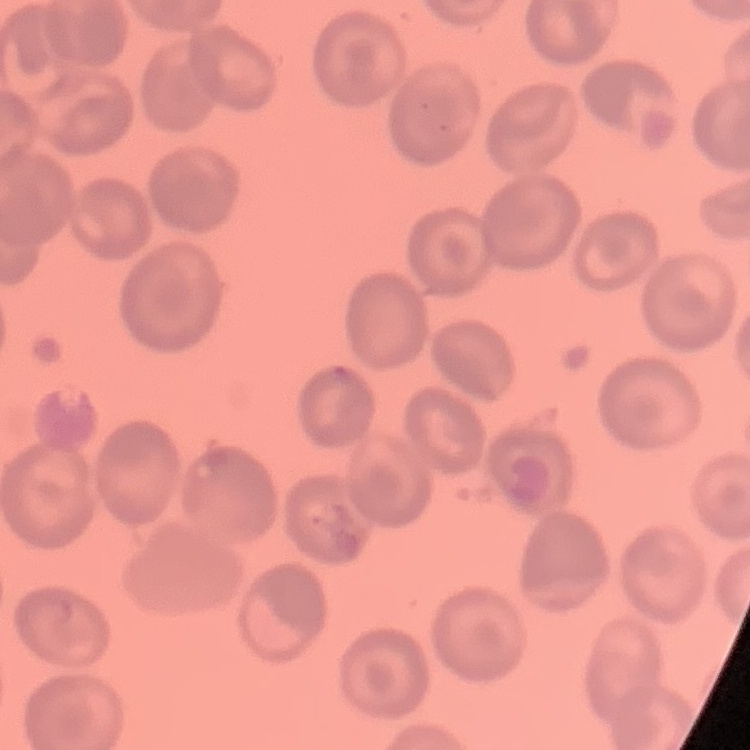 The erythrocytes exhibit no rouleaux formation. One tile cut from a larger photomicrograph. Thin blood smear. Field's or Giemsa stain.